Evaluate for Plasmodium parasites.
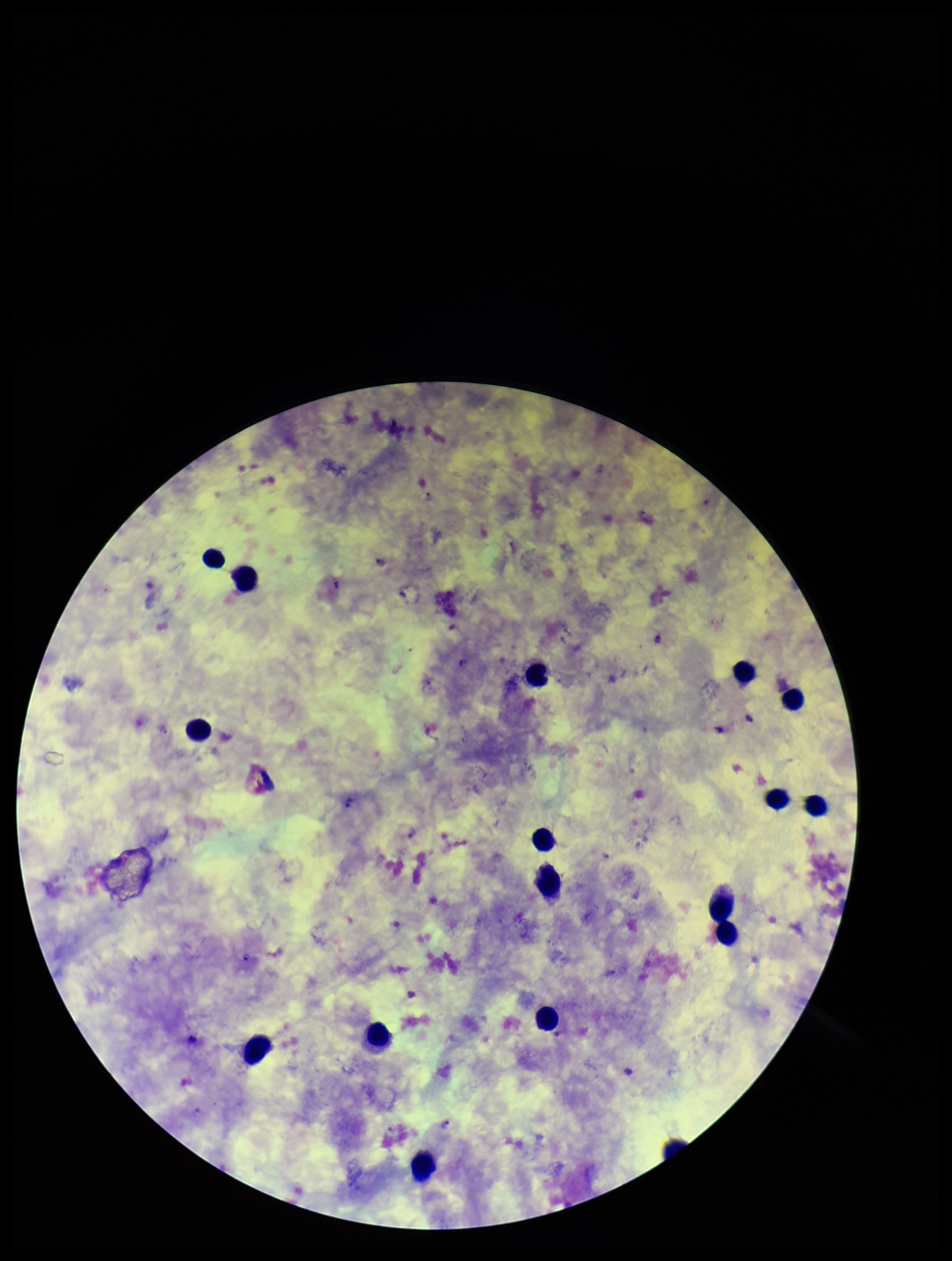

Detected.

{
  "stain": "Giemsa",
  "capture": "smartphone photograph through the microscope eyepiece",
  "species_reported_for_this_patient": "Plasmodium falciparum",
  "parasite_count": 6,
  "image_size": "952×1261 pixels",
  "patient_malaria_status": "infected",
  "field_of_view": "one from this slide",
  "leukocyte_count": 16,
  "preparation": "thick"
}